Locate every Plasmodium parasite.
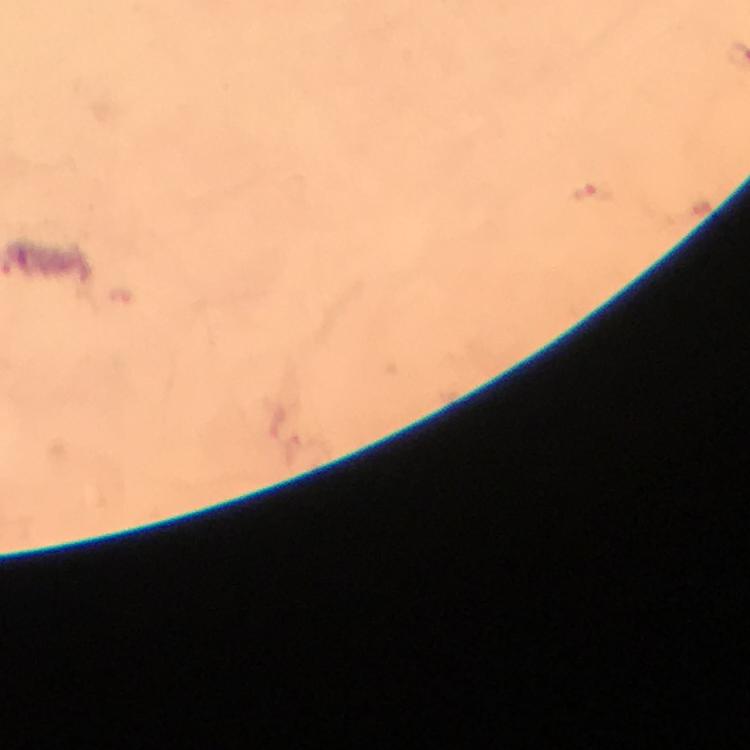

Approximate centers as [x, y] in pixels.
Plasmodium parasites: [593, 197].

Giemsa stain. Photographed through the microscope with a smartphone camera. Thick smear. Cropped region of a single field of view. 100x magnification. From a diagnostic examination for malaria. Immersion oil applied. Image is 750×750 pixels.